Name the cell type shown.
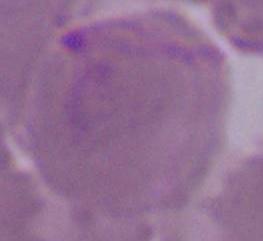
This is an erythrocyte.

Photomicrograph. Captured at 1000x magnification.